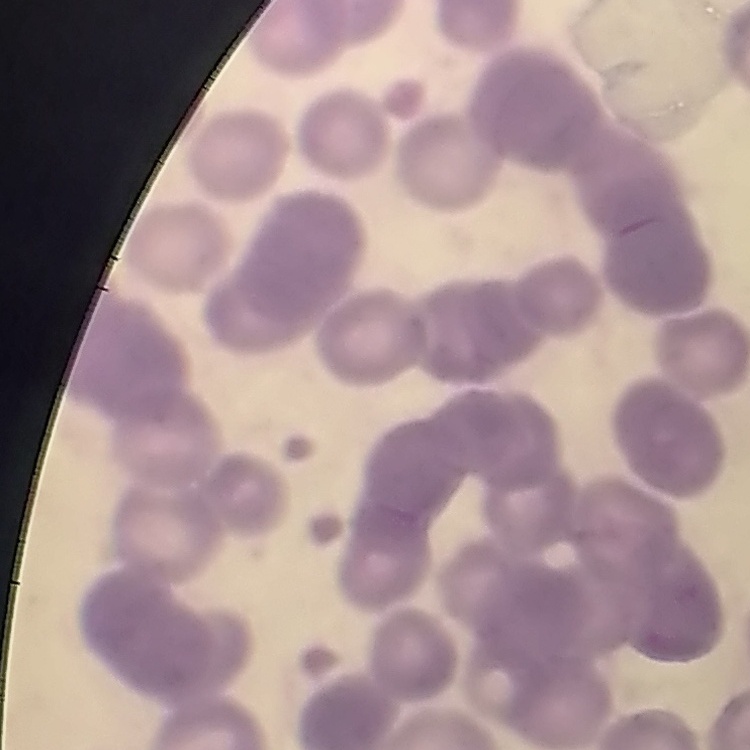
Summary:
  - Erythrocyte morphology: rouleaux formation
  - Stain: Field's or Giemsa
  - Image type: one tile cut from a larger photomicrograph
  - Preparation: thin blood film